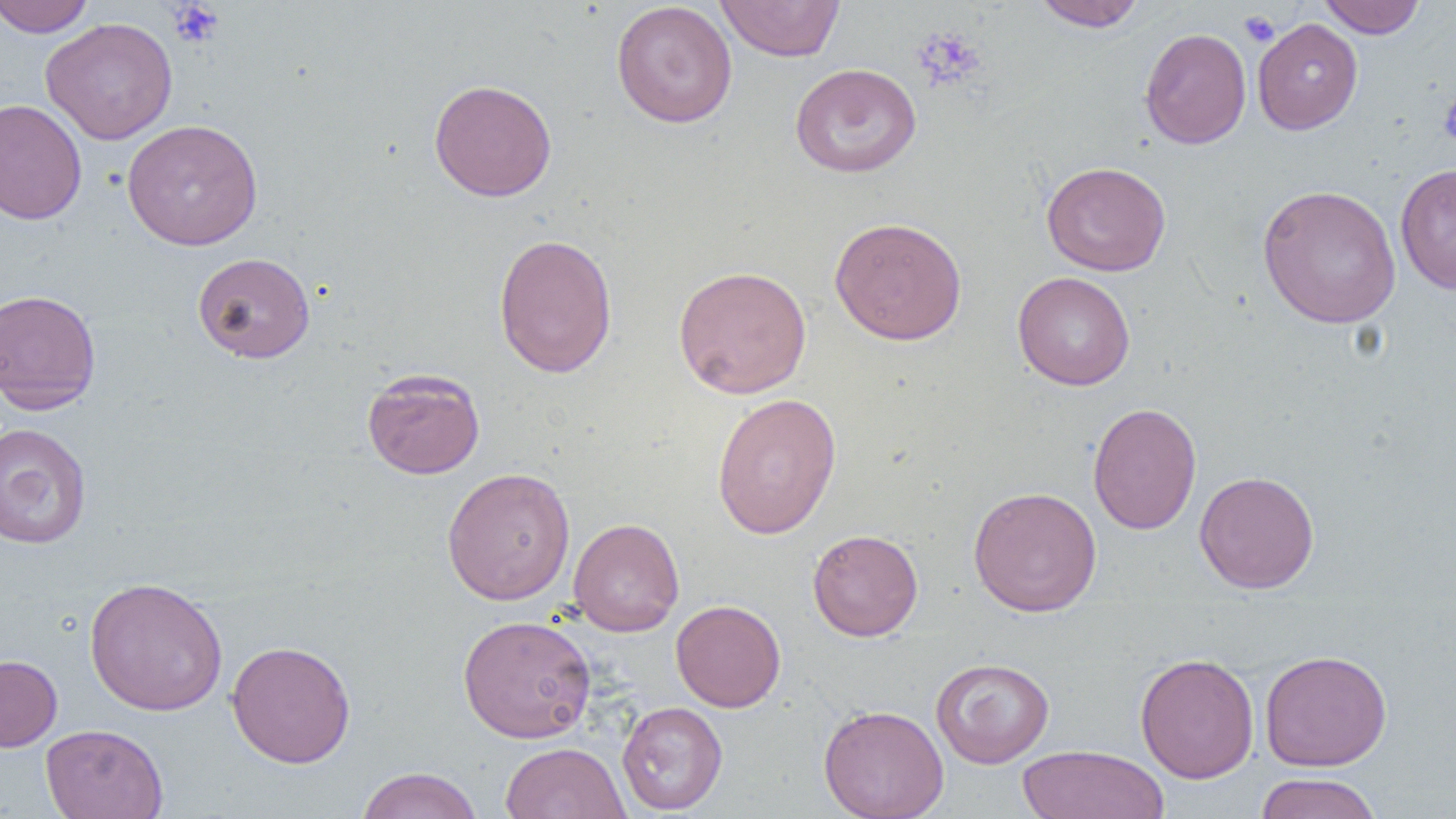

{
  "slide_level_diagnosis": "no evidence of blood parasites",
  "magnification": "1000x",
  "modality": "optical microscopy",
  "platelet_locations": "approximate bounding boxes as named x1/y1/x2/y2 corners in pixels: (x1=167, y1=2, x2=224, y2=49), (x1=1240, y1=10, x2=1279, y2=46), (x1=911, y1=27, x2=987, y2=92), (x1=1439, y1=89, x2=1456, y2=149)",
  "field_of_view": "one of a larger specimen",
  "preparation": "thin blood film",
  "image_size": "1456×819 pixels",
  "uninfected_red_blood_cell_locations": "approximate bounding boxes as named x1/y1/x2/y2 corners in pixels: (x1=0, y1=0, x2=95, y2=37), (x1=1031, y1=0, x2=1148, y2=32), (x1=1318, y1=0, x2=1425, y2=38), (x1=611, y1=1, x2=738, y2=128), (x1=715, y1=1, x2=846, y2=62), (x1=40, y1=17, x2=178, y2=145), (x1=1252, y1=18, x2=1363, y2=134), (x1=1139, y1=27, x2=1251, y2=149), (x1=789, y1=63, x2=921, y2=178), (x1=428, y1=78, x2=557, y2=201), (x1=0, y1=98, x2=87, y2=225), (x1=121, y1=118, x2=263, y2=250), (x1=1041, y1=161, x2=1171, y2=276), (x1=1395, y1=163, x2=1456, y2=295), (x1=1258, y1=184, x2=1401, y2=328), (x1=829, y1=216, x2=967, y2=346), (x1=493, y1=233, x2=618, y2=378), (x1=192, y1=251, x2=315, y2=363), (x1=673, y1=264, x2=812, y2=399), (x1=1012, y1=271, x2=1135, y2=390), (x1=0, y1=288, x2=102, y2=414), (x1=361, y1=367, x2=485, y2=480), (x1=711, y1=392, x2=842, y2=539), (x1=1087, y1=402, x2=1202, y2=535), (x1=0, y1=422, x2=92, y2=549), (x1=441, y1=467, x2=575, y2=604), (x1=1194, y1=470, x2=1320, y2=594), (x1=968, y1=486, x2=1102, y2=617), (x1=568, y1=517, x2=684, y2=636), (x1=808, y1=529, x2=923, y2=642), (x1=84, y1=576, x2=229, y2=717), (x1=671, y1=599, x2=786, y2=712), (x1=457, y1=614, x2=596, y2=743), (x1=227, y1=640, x2=356, y2=768), (x1=1259, y1=649, x2=1393, y2=771), (x1=1134, y1=652, x2=1259, y2=783), (x1=0, y1=655, x2=62, y2=751), (x1=931, y1=657, x2=1054, y2=768), (x1=617, y1=701, x2=728, y2=815), (x1=818, y1=703, x2=949, y2=819), (x1=41, y1=724, x2=168, y2=819), (x1=499, y1=742, x2=630, y2=819), (x1=1017, y1=744, x2=1171, y2=818), (x1=355, y1=767, x2=483, y2=819), (x1=1253, y1=772, x2=1382, y2=819)"
}